Evaluate for malaria.
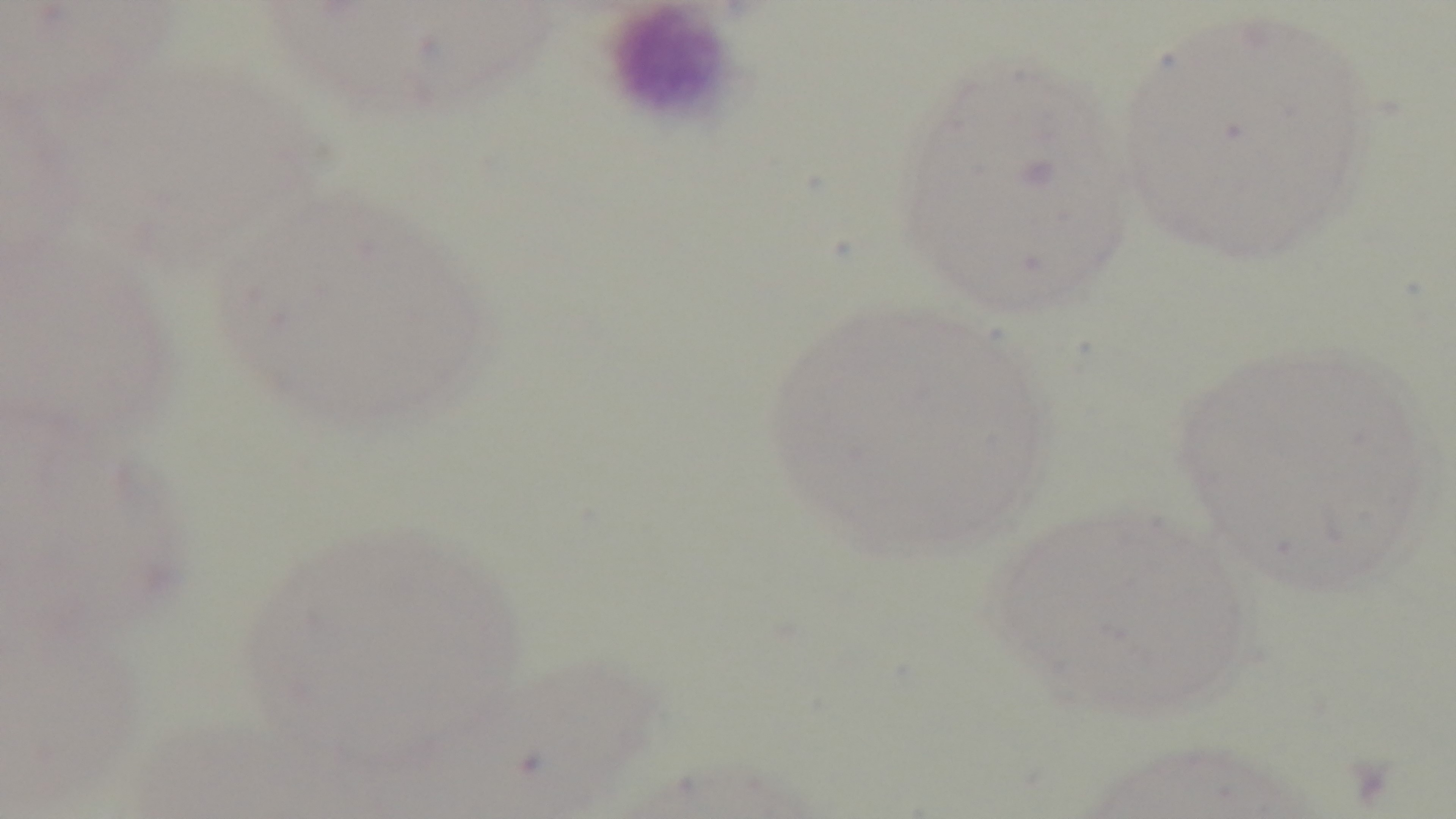

Negative.

Summary:
  - Field of view: one from the slide
  - Objective: 100x oil immersion
  - Stain: Giemsa
  - Capture: mounted 4K digital camera
  - Modality: light microscopy
  - Preparation: thin blood film